State which parasite is depicted.
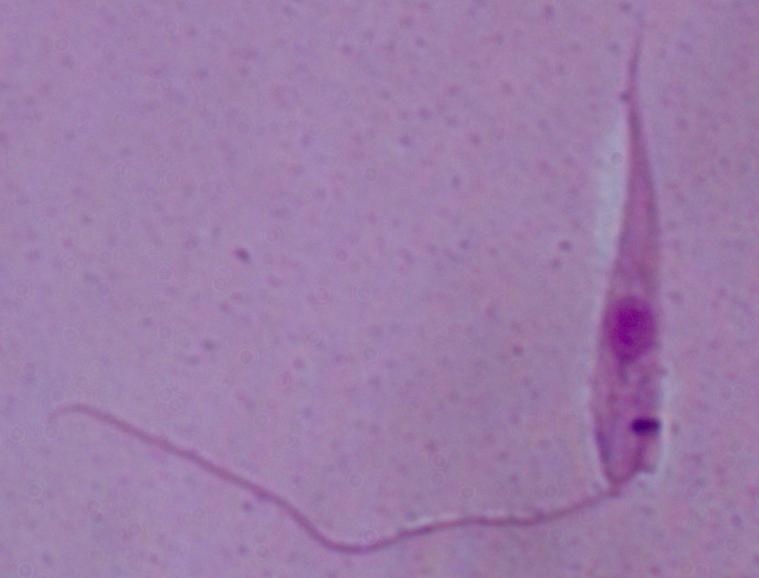
Leishmania.

Micrograph. 1000x magnification.